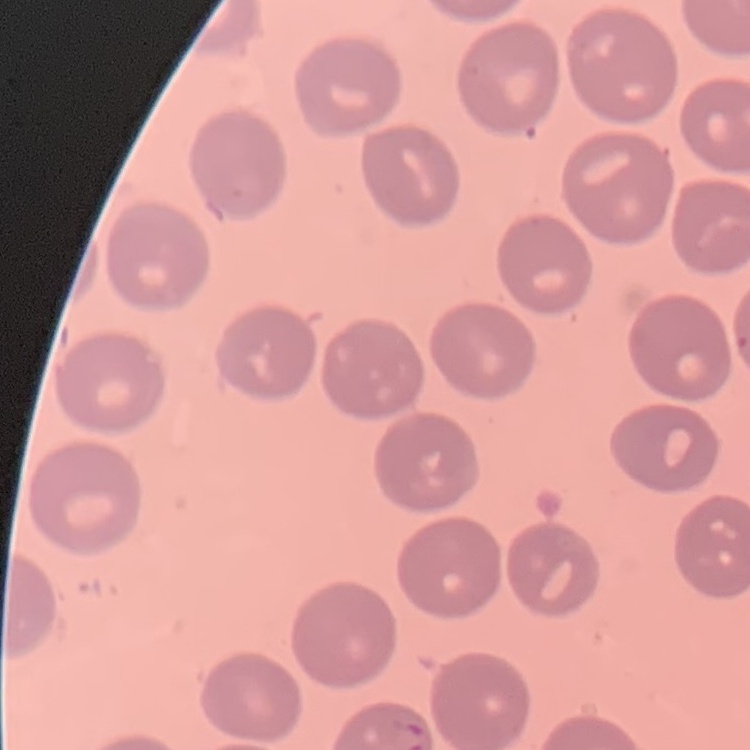
{
  "red_blood_cell_morphology": "no rouleaux formation",
  "stain": "Field's or Giemsa",
  "image_type": "square crop of a larger photomicrograph",
  "preparation": "thin blood smear"
}